Identify the parasite.
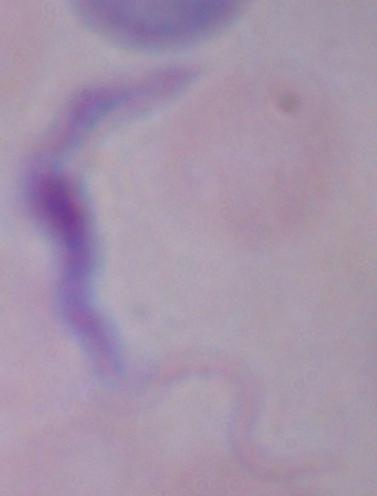
A trypanosome.

Summary:
  - Modality: photomicrograph
  - Magnification: 1000x